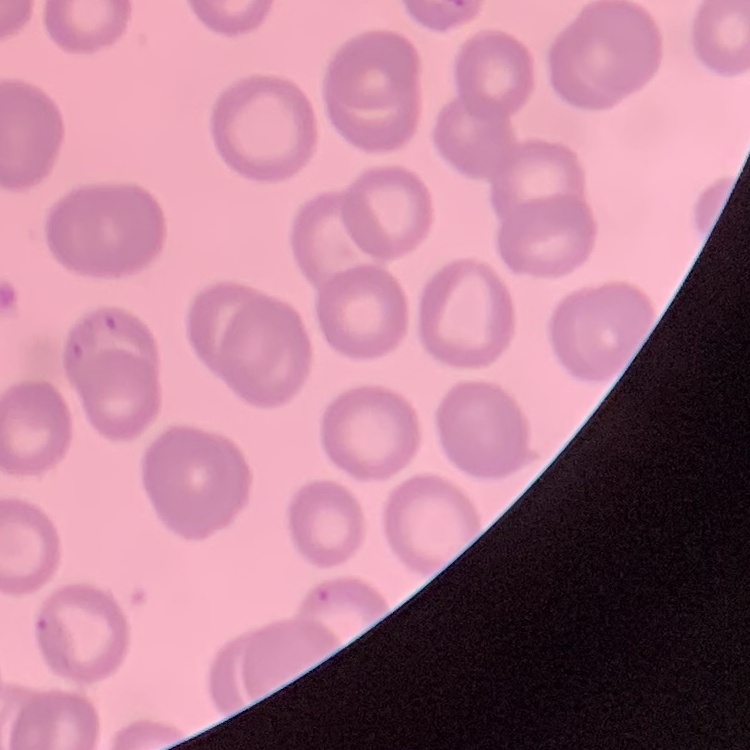
red blood cell morphology = no rouleaux formation
stain = Field's or Giemsa
image type = square crop of a larger photomicrograph
preparation = thin blood smear